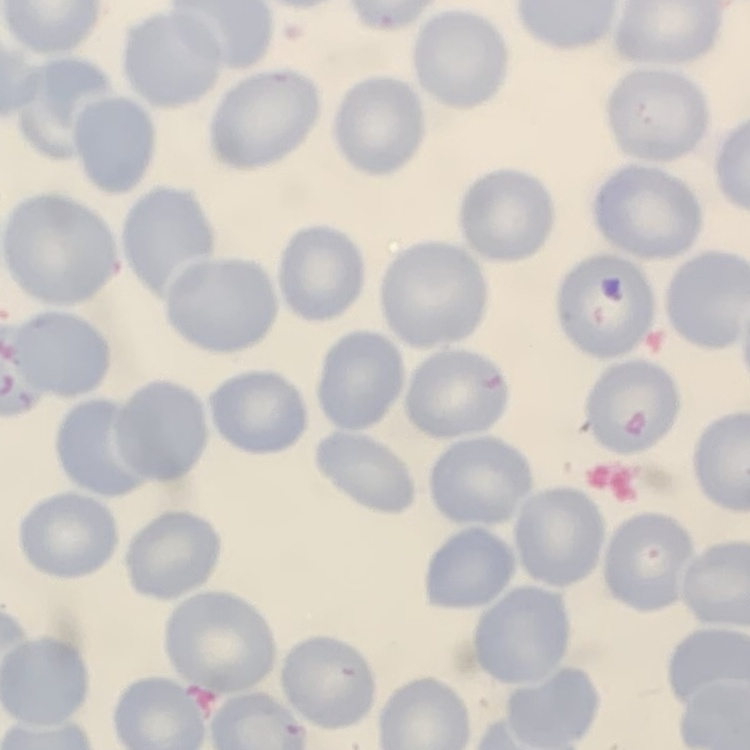 The red blood cells show no rouleaux formation. Stained with either Field's or Giemsa. Thin peripheral smear. One tile cut from a larger photomicrograph.